Locate every Plasmodium parasite and every leukocyte.
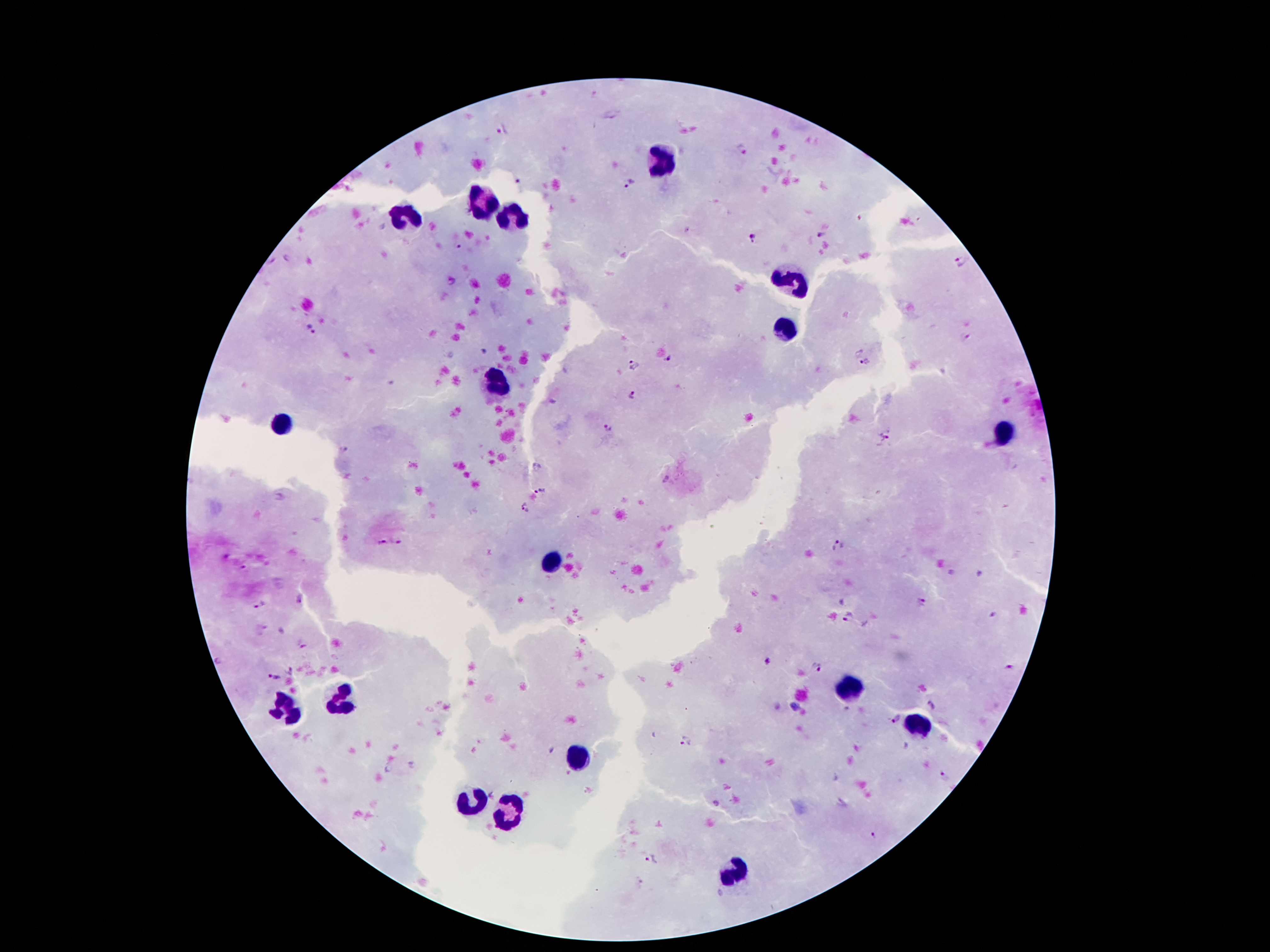
Approximate object centers, in pixels from the top-left corner.
Plasmodium parasites: (x=502, y=130), (x=742, y=149), (x=519, y=182), (x=628, y=185), (x=819, y=234), (x=752, y=237), (x=459, y=246), (x=963, y=260), (x=452, y=280), (x=311, y=329), (x=964, y=335), (x=668, y=358), (x=866, y=362), (x=634, y=365), (x=632, y=395), (x=608, y=426), (x=887, y=433), (x=340, y=451), (x=541, y=490), (x=524, y=509), (x=381, y=542), (x=399, y=543), (x=838, y=545), (x=921, y=603), (x=259, y=605), (x=992, y=614), (x=849, y=615), (x=766, y=662), (x=1009, y=667), (x=290, y=670), (x=817, y=670), (x=274, y=678), (x=935, y=705), (x=896, y=719), (x=684, y=740), (x=947, y=777), (x=716, y=803), (x=874, y=837), (x=650, y=858).
Leukocytes: (x=660, y=160), (x=486, y=203), (x=406, y=216), (x=514, y=218), (x=796, y=279), (x=787, y=330), (x=496, y=382), (x=283, y=425), (x=1005, y=432), (x=557, y=559), (x=848, y=688), (x=346, y=699), (x=285, y=707), (x=914, y=727), (x=580, y=757), (x=471, y=800), (x=507, y=813), (x=731, y=875).

preparation: thick blood film
patient_malaria_status: positive for Plasmodium falciparum
capture: smartphone through the microscope eyepiece
image_size: 1270×952 pixels
field_of_view: single
stain: Giemsa
magnification: 100x